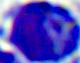
Summary:
  - Magnification: 400x
  - Identification: leukocyte
  - Modality: micrograph